Assess the morphology of the erythrocytes.
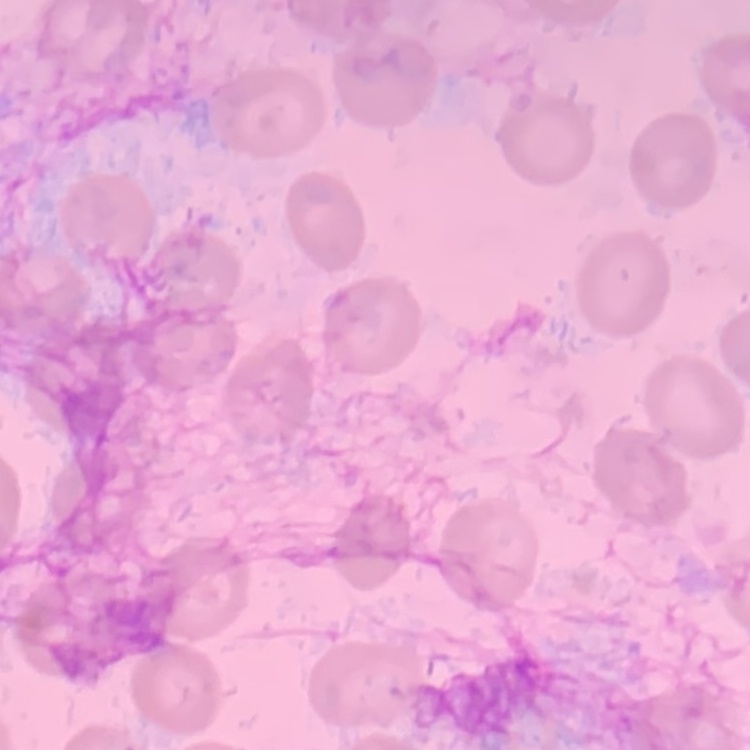
No rouleaux formation.

Thin peripheral smear. Square crop of a larger photomicrograph. Field's or Giemsa stain.